Locate Plasmodium parasites and leukocytes.
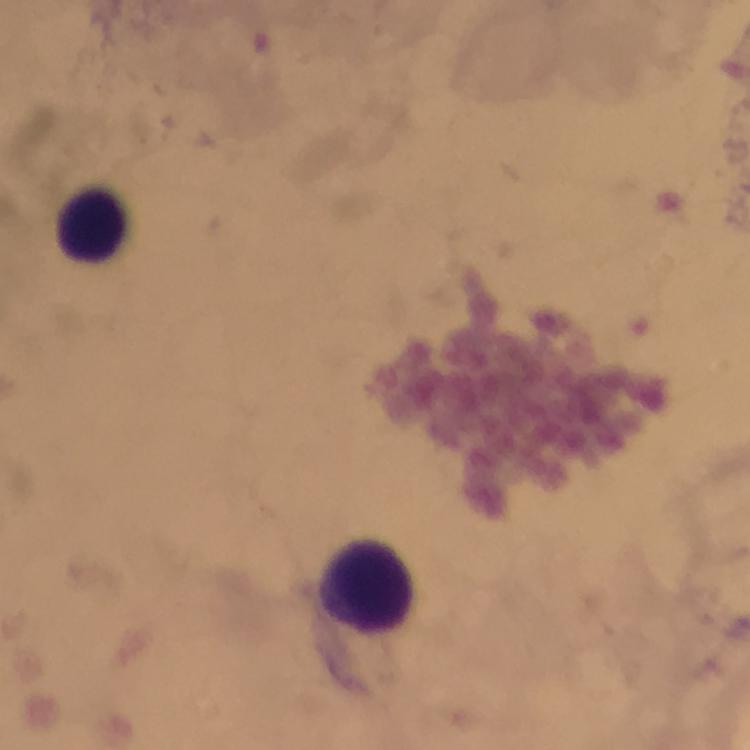
No Plasmodium parasites seen.
Approximate object centers, in pixels from the top-left corner.
Leukocytes: (x=91, y=226), (x=364, y=584).

immersion oil = used
preparation = thick blood smear
cropped from = a single field of view
image size = 750×750 pixels
stain = Giemsa
magnification = 100x
context = from a diagnostic examination for malaria
capture = smartphone photograph through a microscope